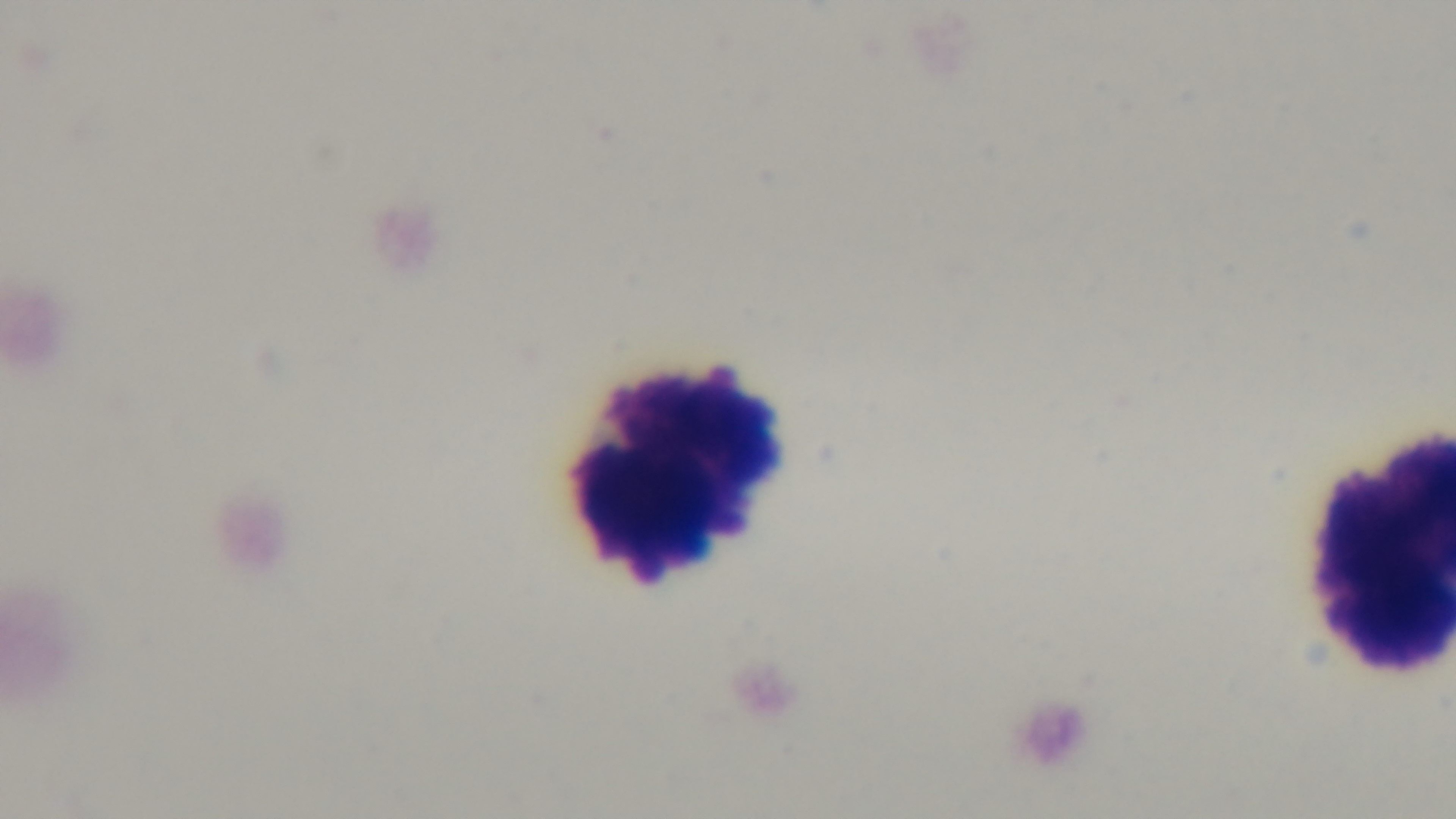

Summary:
  - Capture: mounted 4K digital camera
  - Preparation: thick
  - Modality: light microscopy
  - Field of view: single
  - Objective: 100x oil immersion
  - Stain: Giemsa
  - Malaria status: uninfected